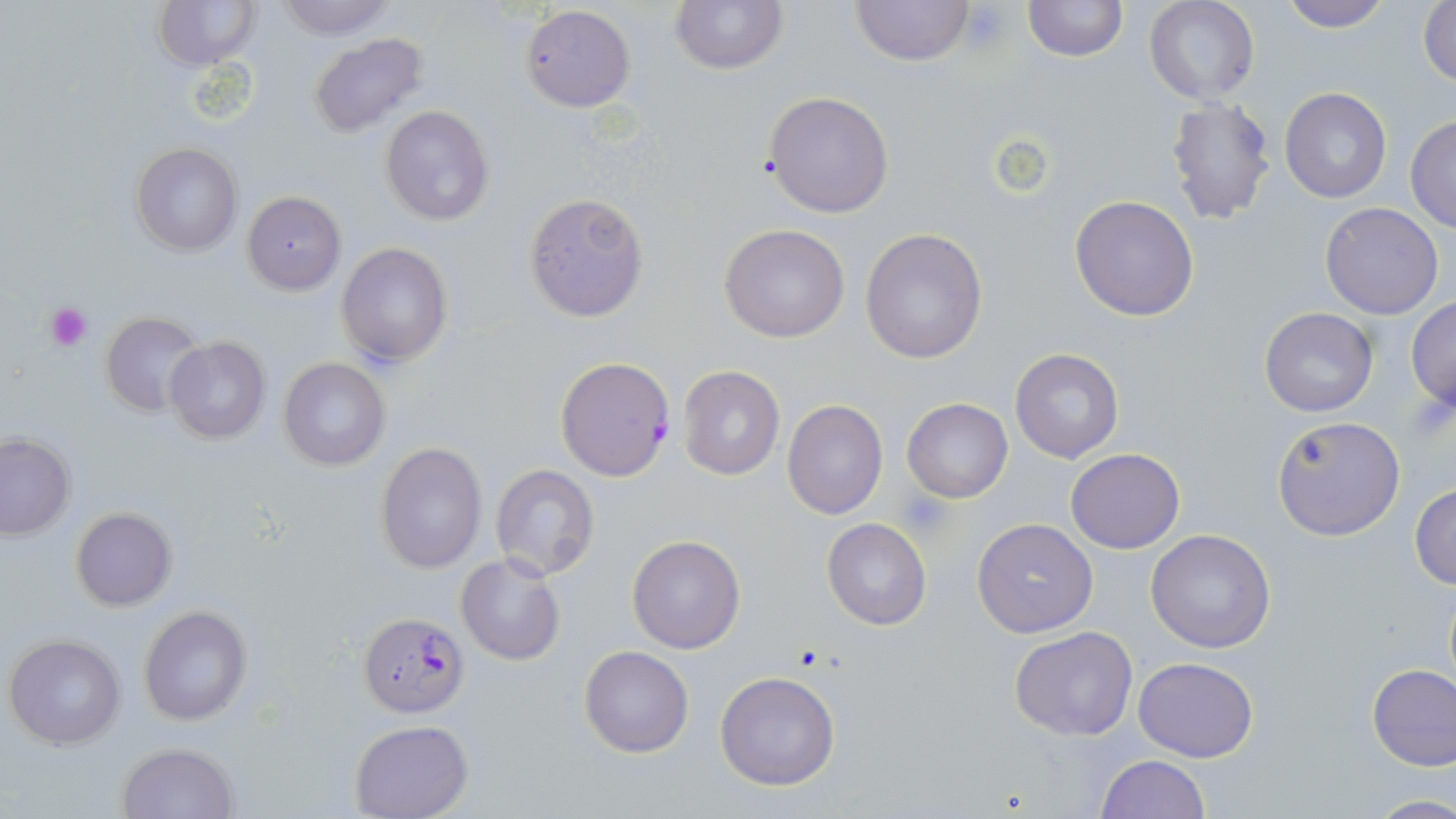 Approximate bounding boxes as (x1,y1)-(x2,y2) corner pairs in pixels. Platelet locations: (959,3)-(1013,48), (44,303)-(91,350), (898,493)-(953,541). Uninfected red blood cell locations: (151,0)-(262,72), (272,0)-(397,39), (670,0)-(786,73), (848,0)-(975,68), (1022,0)-(1127,61), (1144,0)-(1260,105), (1277,0)-(1393,32), (1418,0)-(1456,89), (519,3)-(635,111), (307,32)-(429,137), (1279,86)-(1391,203), (762,90)-(895,218), (1164,94)-(1277,224), (380,105)-(495,227), (1405,116)-(1455,233), (131,142)-(241,256), (241,191)-(346,293), (523,192)-(650,322), (1069,194)-(1200,322), (1318,203)-(1444,319), (719,223)-(851,343), (859,228)-(988,364), (337,242)-(453,367), (1406,297)-(1456,408), (1259,307)-(1378,417), (100,310)-(206,413), (163,335)-(272,444), (1010,348)-(1124,463), (279,357)-(390,471), (678,364)-(785,481), (782,398)-(888,519), (902,398)-(1013,503), (1271,415)-(1406,540), (0,432)-(75,539), (375,441)-(487,576), (1066,449)-(1184,553), (489,464)-(599,582), (1410,484)-(1456,588), (70,506)-(177,610), (822,518)-(931,630), (972,518)-(1098,638), (1145,529)-(1276,654), (627,535)-(746,655), (456,553)-(566,666), (137,605)-(252,727), (1010,625)-(1138,741), (4,634)-(127,751), (579,645)-(694,756), (1132,656)-(1259,762), (1365,662)-(1456,771), (714,672)-(840,791), (349,719)-(475,818), (116,742)-(238,819), (1096,755)-(1210,818), (1368,794)-(1456,818). Plasmodium falciparum-infected red blood cell locations: (554,355)-(676,483), (359,610)-(470,716). Slide-level diagnosis: Plasmodium falciparum. Thin blood smear. 1000x magnification. May-Grünwald-Giemsa stain. Light microscopy. Image is 1456×819 pixels. One field of a larger specimen.